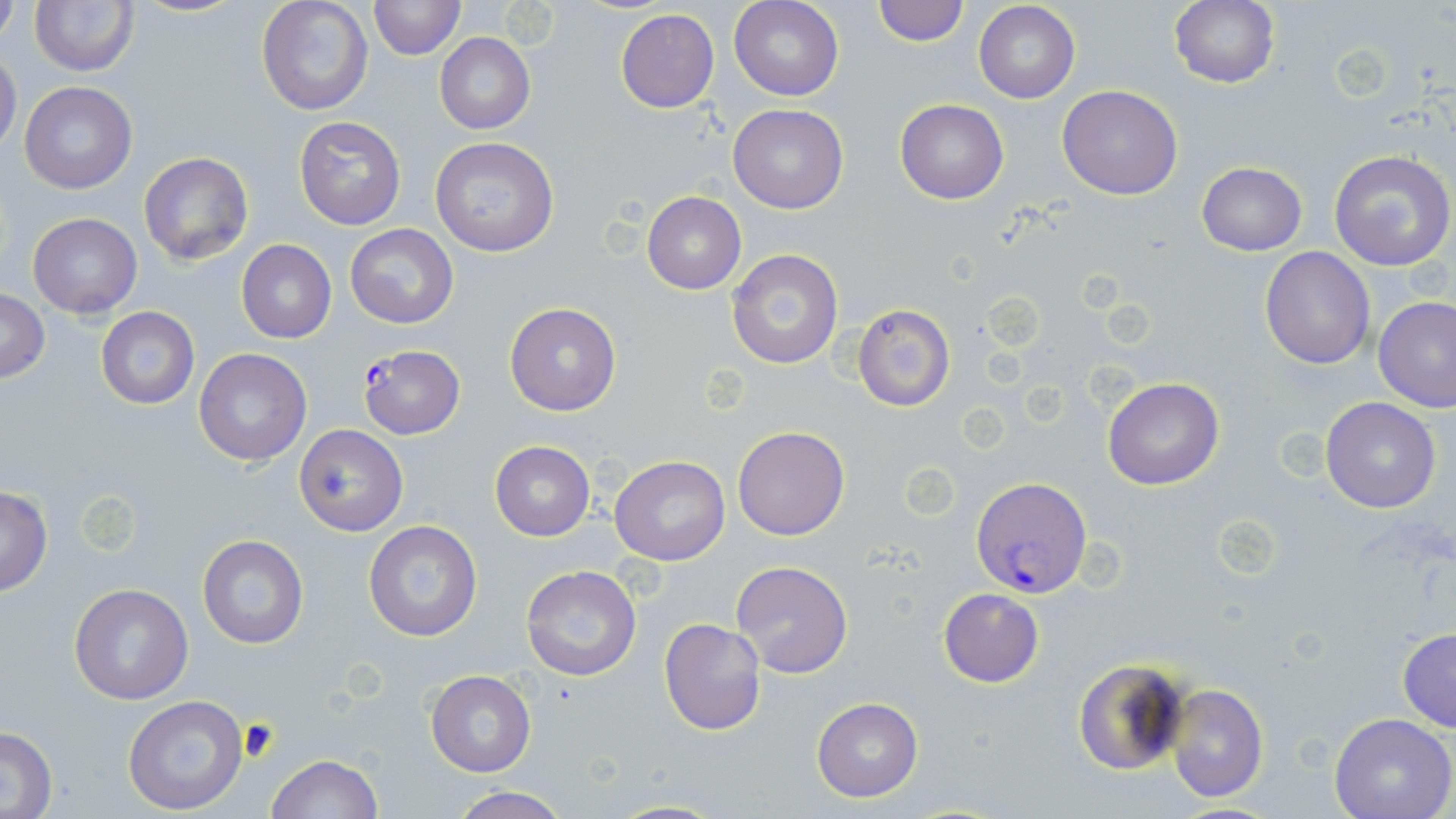

slide-level diagnosis = Plasmodium falciparum
field of view = one of a larger specimen
Plasmodium falciparum-infected red blood cell locations = approximate bounding boxes as [x1, y1, x2, y2] in pixels: [355, 345, 466, 443], [970, 478, 1092, 596]
stain = May-Grünwald-Giemsa
preparation = thin blood smear
magnification = 1000x
uninfected red blood cell locations = approximate bounding boxes as [x1, y1, x2, y2] in pixels: [131, 0, 248, 17], [257, 0, 373, 115], [369, 0, 464, 60], [729, 0, 844, 102], [972, 0, 1080, 104], [30, 1, 138, 75], [872, 1, 969, 48], [1169, 1, 1279, 90], [0, 5, 19, 50], [615, 9, 719, 113], [434, 33, 535, 134], [0, 50, 22, 155], [20, 81, 136, 194], [1058, 85, 1183, 200], [895, 98, 1009, 203], [728, 103, 847, 215], [294, 115, 405, 230], [430, 137, 559, 258], [137, 150, 253, 266], [1328, 150, 1456, 272], [1196, 162, 1307, 255], [643, 191, 745, 293], [28, 212, 142, 317], [344, 224, 459, 330], [236, 240, 336, 344], [1260, 246, 1375, 369], [726, 247, 845, 370], [1, 289, 49, 383], [1373, 295, 1456, 411], [504, 302, 623, 417], [852, 304, 957, 413], [95, 307, 199, 410], [194, 348, 312, 467], [1102, 377, 1224, 490], [1320, 397, 1441, 513], [294, 424, 408, 536], [733, 425, 850, 541], [490, 442, 595, 541], [610, 456, 729, 567], [0, 487, 54, 594], [363, 520, 484, 641], [197, 535, 309, 649], [730, 561, 854, 679], [519, 566, 642, 683], [68, 582, 194, 704], [937, 587, 1044, 687], [659, 618, 767, 736], [1397, 628, 1456, 733], [1070, 657, 1189, 777], [426, 671, 535, 775], [1163, 682, 1268, 802], [121, 694, 249, 815], [812, 697, 923, 802], [1329, 711, 1455, 819], [0, 726, 58, 817], [266, 753, 382, 819], [448, 786, 572, 819]
image size = 1456×819 pixels
modality = light microscopy